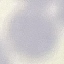

Summary:
  - Result: negative for malaria parasites
  - Image type: automatically extracted cell patch, resized to 64 × 64 pixels
  - Preparation: thin smear
  - Stain: Giemsa
  - Capture: smartphone camera at the microscope eyepiece